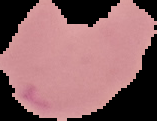
Summary:
  - Image type: cell region segmented out of the field of view; surrounding area masked to black
  - Result: malaria parasites detected
  - Preparation: thin blood smear
  - Image size: 157×121 pixels